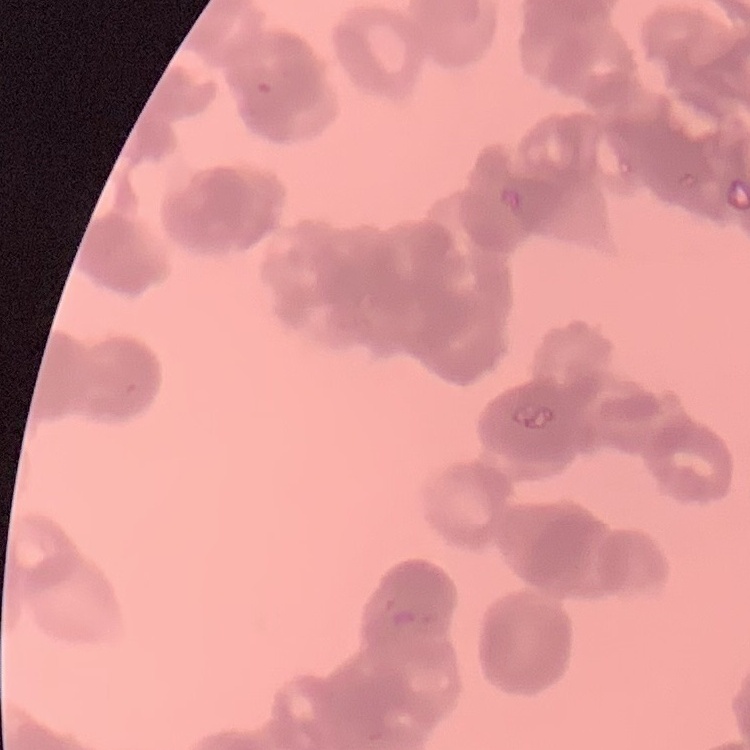
Summary:
  - Erythrocyte morphology: rouleaux formation
  - Image type: square crop of a larger photomicrograph
  - Preparation: thin peripheral smear
  - Stain: Field's or Giemsa